Report the malaria status of this cell.
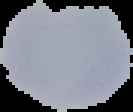

Uninfected.

image_size: 133×112 pixels
preparation: thin blood film
image_type: segmented cell region on a black background